Describe the morphology of the erythrocytes.
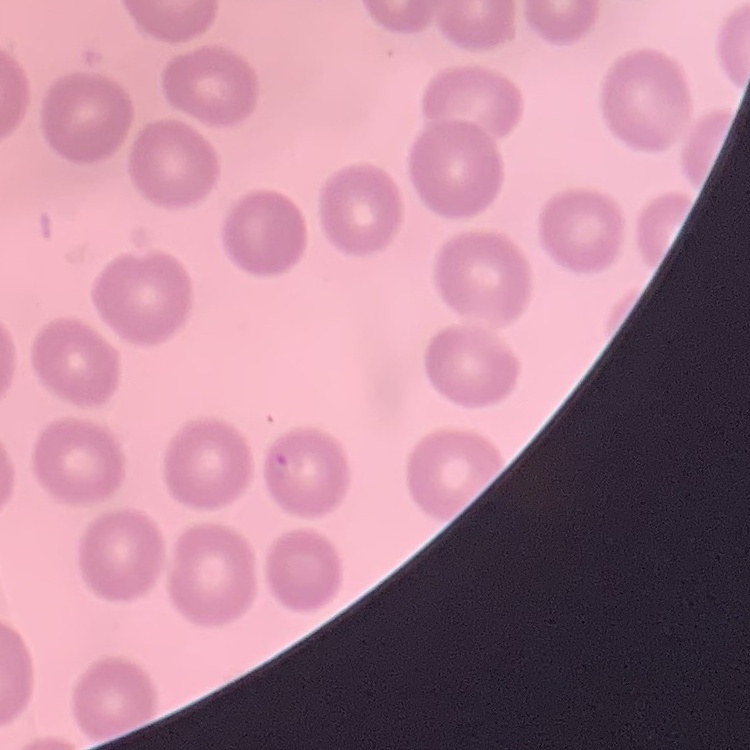

They show no rouleaux formation.

Field's or Giemsa stain. One tile cut from a larger photomicrograph. Thin blood smear.